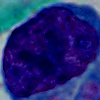
Captured at 1000x magnification. A leukocyte is shown. Micrograph.